Locate and identify every blood parasite.
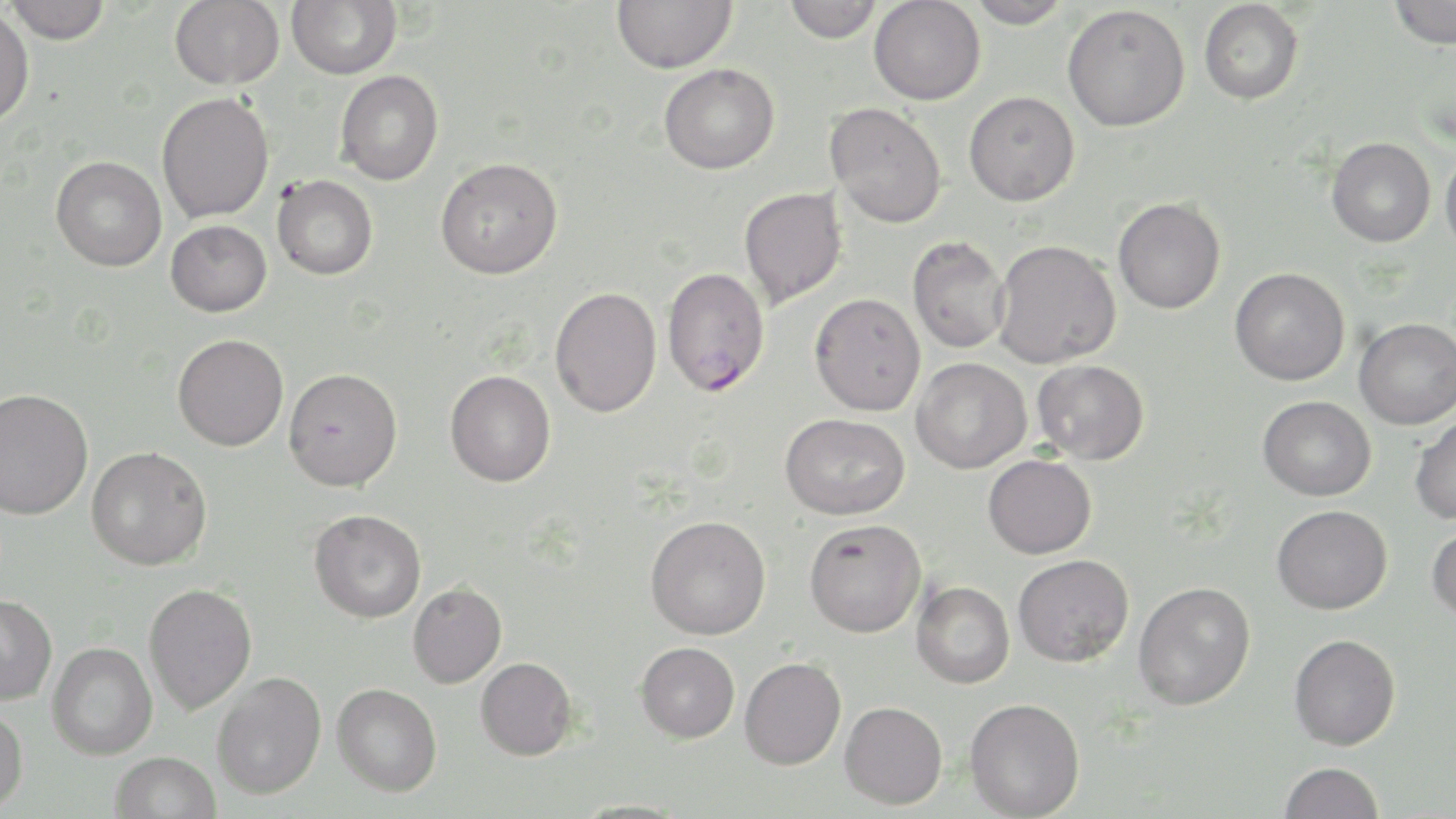

Approximate bounding boxes as (x1, y1, x2, y2) in pixels.
Plasmodium falciparum-infected red blood cells: (661, 267, 770, 397).
No Plasmodium ovale, Plasmodium malariae, Plasmodium vivax, Babesia divergens, or Trypanosoma brucei observed.

Summary:
  - Uninfected red blood cell locations: (5, 0, 111, 43), (169, 0, 284, 89), (286, 0, 402, 79), (611, 0, 737, 74), (782, 0, 884, 43), (869, 0, 985, 105), (966, 0, 1072, 28), (1199, 0, 1304, 105), (1388, 0, 1456, 49), (1062, 4, 1190, 132), (0, 6, 34, 128), (659, 63, 779, 174), (335, 70, 444, 186), (964, 91, 1079, 206), (156, 92, 274, 224), (825, 102, 947, 228), (1327, 137, 1435, 247), (1440, 146, 1456, 257), (51, 156, 167, 271), (436, 157, 563, 279), (272, 175, 378, 280), (739, 187, 846, 309), (1113, 197, 1226, 314), (165, 220, 272, 317), (907, 235, 1011, 353), (992, 240, 1121, 369), (1230, 267, 1350, 386), (550, 287, 662, 417), (810, 293, 925, 416), (1354, 318, 1456, 429), (172, 334, 288, 451), (911, 358, 1031, 474), (1032, 359, 1149, 465), (283, 368, 402, 491), (445, 370, 556, 487), (0, 388, 93, 520), (1258, 396, 1375, 501), (780, 413, 909, 520), (1409, 414, 1456, 525), (87, 446, 212, 570), (983, 454, 1096, 558), (1272, 505, 1392, 614), (309, 509, 426, 623), (645, 515, 771, 639), (804, 518, 926, 637), (1427, 524, 1456, 623), (1013, 554, 1133, 667), (911, 580, 1015, 688), (408, 582, 507, 688), (1133, 582, 1256, 710), (143, 583, 257, 715), (0, 593, 57, 705), (1289, 633, 1401, 750), (47, 642, 157, 760), (635, 642, 740, 742), (475, 657, 578, 760), (740, 657, 846, 769), (212, 672, 326, 799), (332, 683, 442, 796), (964, 697, 1085, 819), (839, 701, 947, 809), (0, 704, 28, 813), (110, 751, 221, 819), (1279, 762, 1384, 819), (568, 799, 691, 818)
  - Slide-level diagnosis: Plasmodium falciparum
  - Field of view: single
  - Modality: light microscopy
  - Stain: May-Grünwald-Giemsa
  - Preparation: thin blood film
  - Image size: 1456×819 pixels
  - Magnification: 1000x